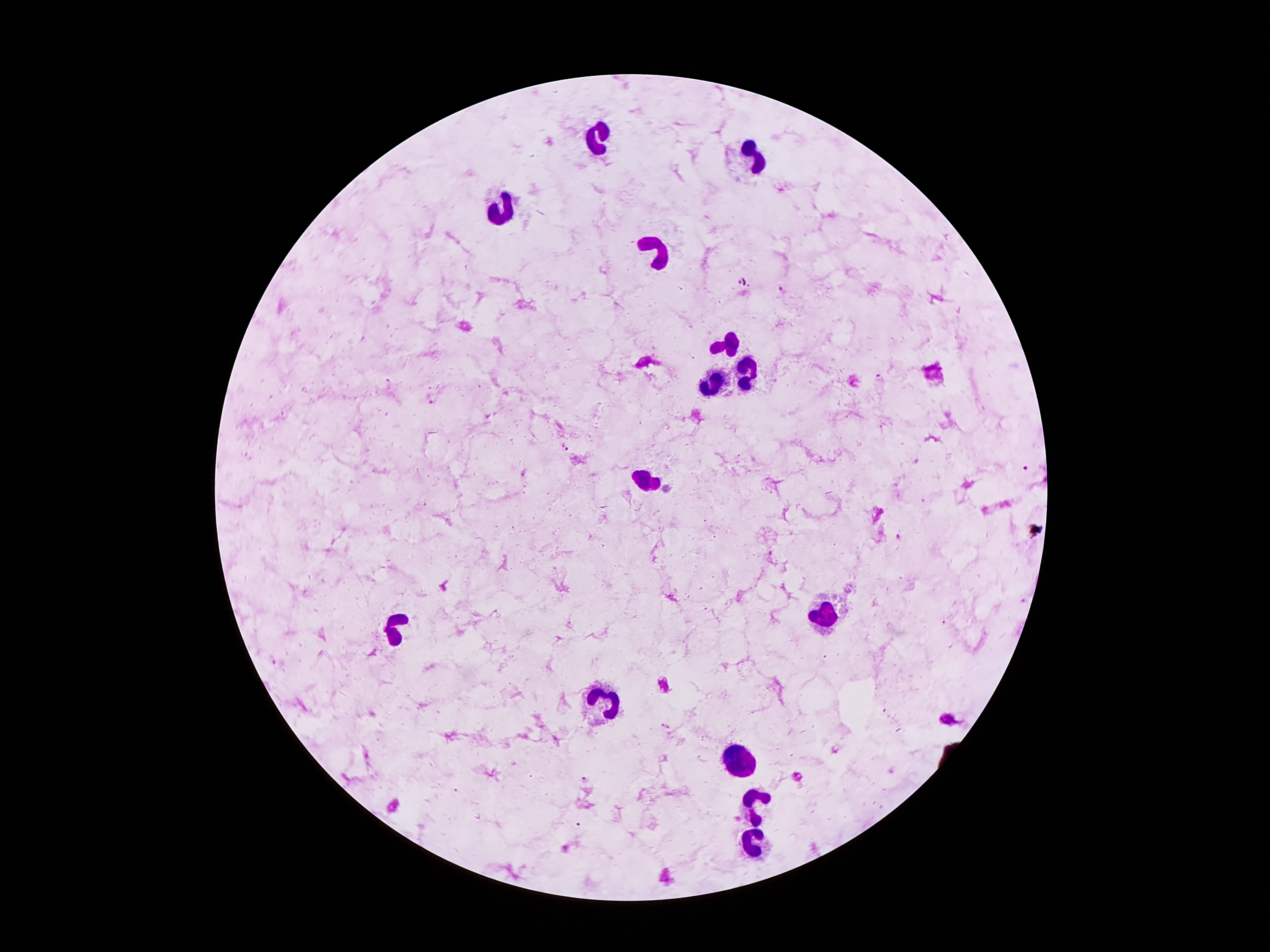
Approximate centers as (x, y) in pixels.
Summary:
  - Plasmodium parasite locations: (783, 290), (880, 377), (431, 398), (565, 448), (1027, 468), (898, 537), (666, 725), (584, 779)
  - Leukocyte locations: (600, 133), (747, 162), (501, 209), (660, 257), (728, 343), (744, 372), (709, 385), (648, 480), (826, 618), (398, 629), (610, 698), (740, 757), (753, 799), (751, 841)
  - Stain: Giemsa
  - Magnification: 100x
  - Capture: smartphone camera through the microscope eyepiece
  - Field of view: one from this slide
  - Preparation: thick blood smear
  - Patient malaria status: infected with Plasmodium falciparum
  - Image size: 1270×952 pixels